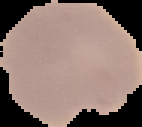
{
  "image_type": "cell region segmented out of the field of view; surrounding area masked to black",
  "preparation": "thin blood film",
  "result": "Plasmodium parasites identified",
  "image_size": "142×127 pixels"
}